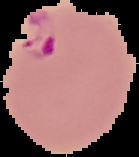

Summary:
  - Result: malaria parasites detected
  - Preparation: thin blood film
  - Image type: segmented cell region on a black background
  - Image size: 139×157 pixels